Identify the parasite.
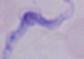

A trypanosome.

{
  "magnification": "1000x",
  "modality": "micrograph"
}